State the blood parasite species.
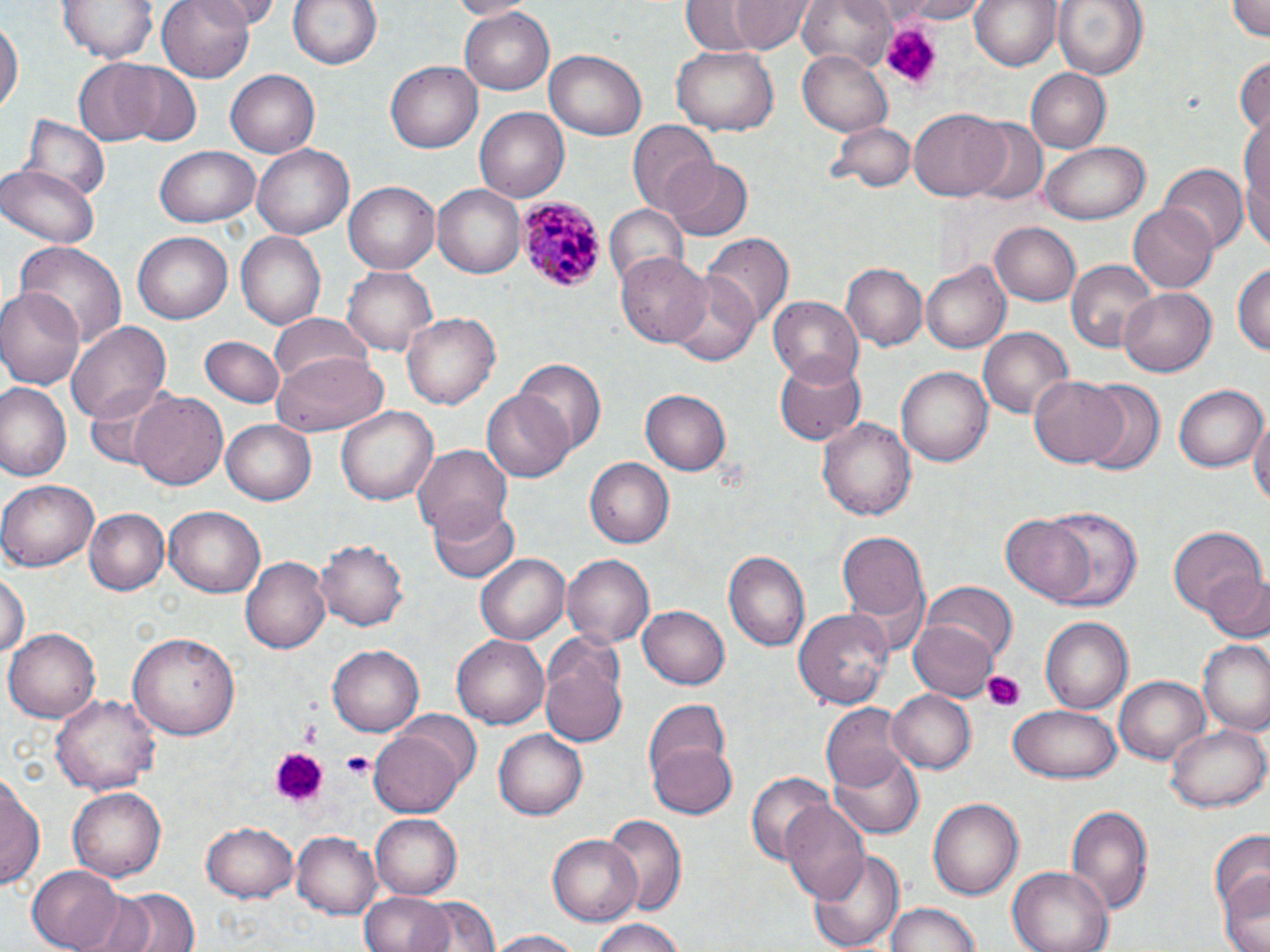

Plasmodium malariae.

Summary:
  - Coordinate format: approximate bounding boxes as (x1, y1, x2, y2) in pixels
  - Platelet locations: (877, 22, 940, 86), (982, 669, 1027, 711), (296, 722, 323, 743), (270, 746, 327, 805), (339, 750, 373, 780)
  - Plasmodium malariae-infected red blood cell locations: (517, 197, 604, 293)
  - Uninfected red blood cell locations: (61, 0, 155, 64), (158, 0, 258, 82), (201, 0, 287, 26), (285, 0, 385, 71), (450, 0, 526, 18), (731, 0, 811, 53), (798, 0, 898, 75), (883, 0, 998, 23), (969, 0, 1062, 71), (1054, 0, 1147, 82), (1226, 0, 1270, 41), (679, 2, 760, 52), (459, 6, 558, 94), (0, 18, 22, 116), (671, 46, 779, 135), (799, 50, 893, 136), (545, 51, 648, 140), (1234, 54, 1270, 138), (74, 58, 166, 146), (112, 60, 202, 144), (386, 60, 482, 153), (1027, 68, 1110, 152), (226, 69, 320, 156), (474, 107, 569, 201), (909, 108, 1009, 201), (23, 115, 109, 202), (828, 119, 914, 193), (967, 119, 1048, 206), (1240, 121, 1270, 245), (629, 123, 719, 216), (1039, 142, 1151, 225), (254, 145, 354, 239), (155, 146, 261, 228), (662, 159, 752, 241), (0, 164, 98, 247), (1162, 164, 1245, 250), (344, 181, 440, 274), (433, 184, 526, 278), (1128, 202, 1220, 293), (603, 205, 687, 290), (991, 222, 1081, 307), (235, 231, 326, 331), (132, 233, 232, 323), (704, 234, 792, 332), (13, 243, 127, 355), (615, 251, 711, 347), (1067, 259, 1157, 353), (1235, 261, 1270, 359), (842, 262, 927, 350), (921, 263, 1012, 354), (343, 266, 436, 355), (667, 271, 761, 366), (0, 284, 85, 394), (1118, 284, 1216, 374), (769, 297, 864, 386), (401, 311, 501, 411), (270, 314, 372, 398), (67, 323, 171, 426), (979, 327, 1072, 420), (202, 335, 284, 406), (273, 354, 384, 437), (772, 355, 864, 445), (516, 359, 605, 458), (896, 364, 993, 467), (1029, 375, 1128, 467), (1078, 381, 1164, 473), (0, 382, 73, 483), (82, 383, 186, 470), (1172, 383, 1265, 471), (483, 388, 576, 481), (640, 390, 732, 475), (132, 392, 229, 492), (335, 405, 438, 508), (1250, 409, 1270, 510), (818, 415, 916, 523), (222, 421, 316, 504), (412, 445, 513, 535), (584, 457, 674, 548), (0, 478, 100, 571), (428, 500, 518, 584), (1034, 505, 1144, 612), (163, 506, 265, 597), (85, 508, 170, 593), (1001, 515, 1097, 606), (1167, 522, 1266, 621), (837, 532, 930, 632), (315, 538, 408, 631), (724, 550, 811, 653), (476, 552, 570, 644), (563, 554, 654, 649), (241, 557, 334, 654), (1205, 567, 1269, 643), (1, 572, 27, 661), (920, 583, 1015, 668), (638, 607, 730, 689), (795, 607, 892, 711), (1040, 616, 1133, 714), (908, 619, 1001, 700), (7, 628, 99, 722), (130, 630, 240, 739), (452, 631, 549, 726), (1197, 640, 1270, 735), (538, 642, 628, 749), (328, 645, 423, 736), (1116, 676, 1208, 764), (889, 691, 976, 774), (52, 692, 161, 797), (644, 698, 735, 796), (821, 702, 909, 790), (1007, 705, 1121, 784), (1164, 721, 1270, 813), (370, 728, 464, 817), (494, 729, 587, 819), (647, 742, 739, 819), (830, 752, 925, 838), (746, 769, 833, 867), (1, 772, 43, 894), (69, 786, 166, 880), (928, 796, 1024, 900), (780, 800, 870, 904), (1064, 804, 1154, 917), (371, 813, 462, 898), (602, 814, 687, 921), (202, 821, 298, 900), (1208, 829, 1269, 925), (292, 832, 379, 917), (548, 834, 641, 926), (810, 847, 907, 950), (27, 865, 124, 951), (1010, 865, 1114, 952), (1216, 872, 1270, 952), (110, 887, 199, 952), (75, 893, 161, 952), (361, 893, 452, 952), (414, 895, 499, 952), (884, 901, 981, 951), (590, 917, 694, 952), (482, 930, 591, 952)
  - Field of view: one of a larger specimen
  - Stain: May-Grünwald-Giemsa
  - Magnification: 1000x
  - Modality: optical microscopy
  - Preparation: thin blood film
  - Image size: 1270×952 pixels